Give the position of every Plasmodium parasite visible.
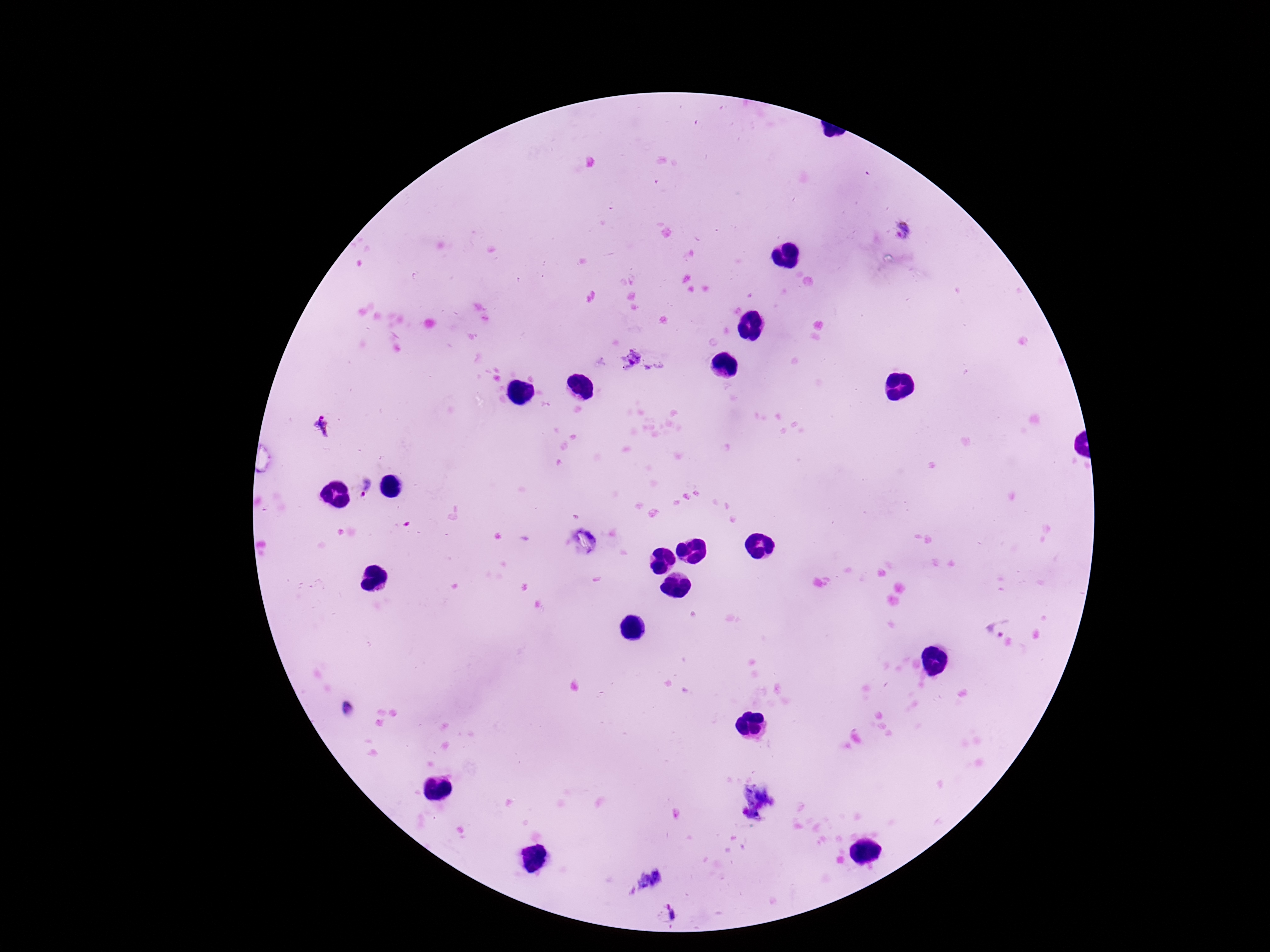

Approximate centers as [x, y] in pixels.
Plasmodium parasites: [902, 229], [322, 427], [366, 487], [1003, 629].

Summary:
  - Stain: Giemsa
  - Magnification: 100x
  - Preparation: thick peripheral-blood smear
  - Field of view: single
  - Image size: 1270×952 pixels
  - Capture: smartphone camera through the microscope eyepiece
  - Patient malaria status: positive